Give the position of every Plasmodium parasite visible.
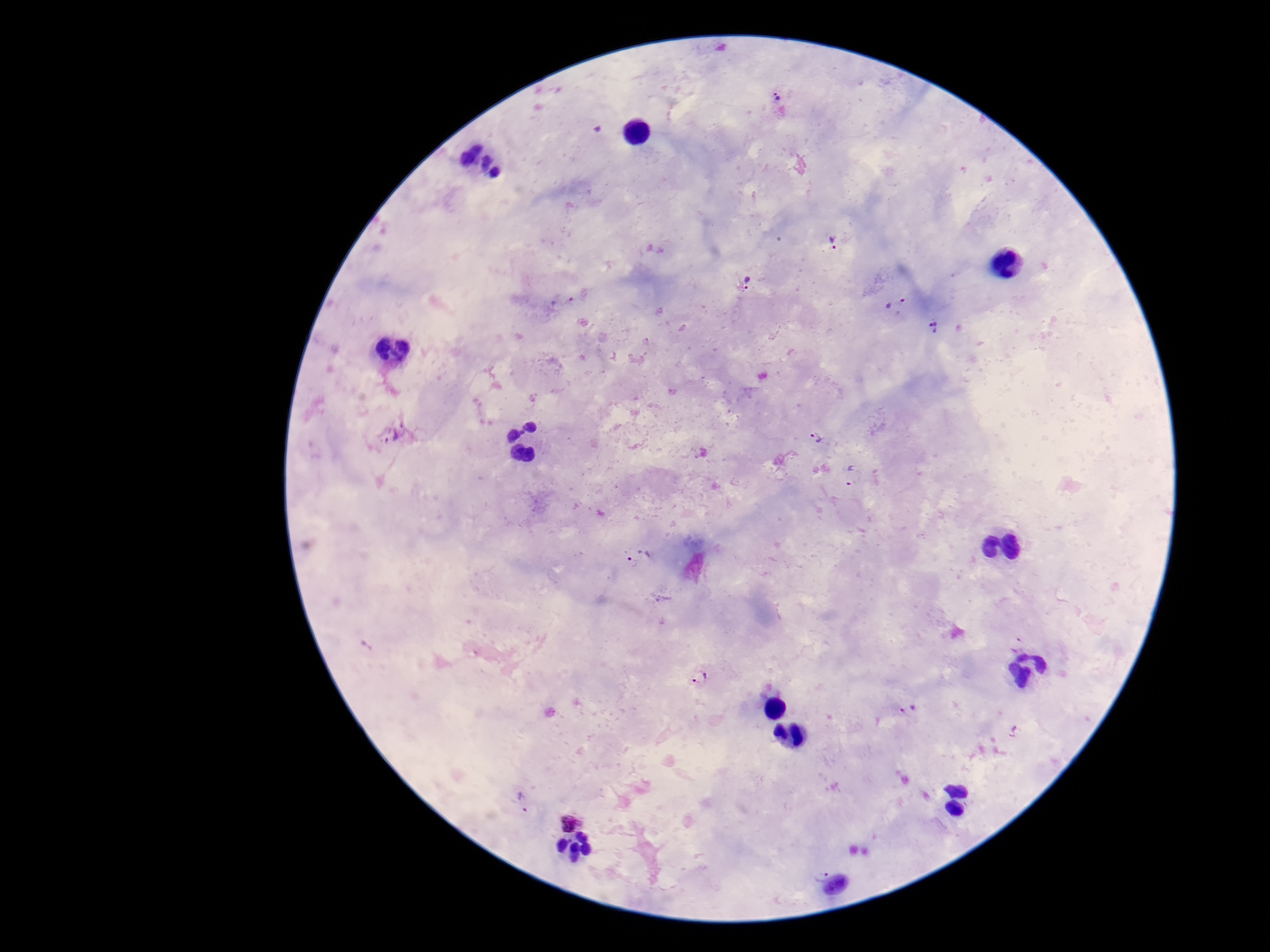
Approximate object centers, in pixels from the top-left corner.
Plasmodium parasites: (x=778, y=98), (x=833, y=242), (x=747, y=281), (x=563, y=302), (x=895, y=305), (x=934, y=327), (x=395, y=435), (x=817, y=437), (x=853, y=475), (x=642, y=556), (x=701, y=677), (x=909, y=709), (x=1015, y=731), (x=523, y=802), (x=569, y=822), (x=821, y=874).

Summary:
  - Patient malaria status: infected
  - Field of view: single
  - Preparation: thick peripheral-blood smear
  - Capture: smartphone camera through the microscope eyepiece
  - Stain: Giemsa
  - Image size: 1270×952 pixels
  - Magnification: 100x